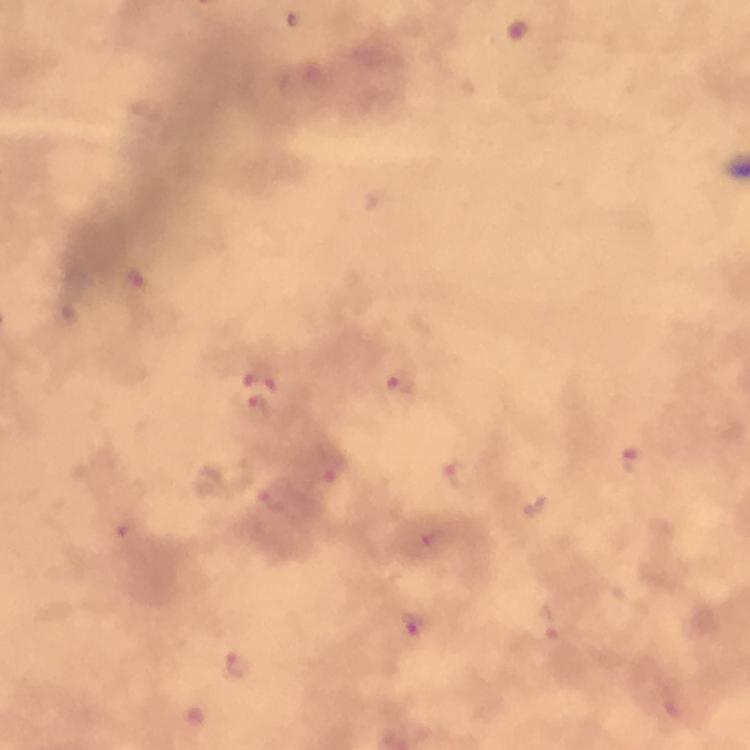
Approximate centers as {x, y} in pixels.
Summary:
  - Malaria parasite locations: {518, 29}, {133, 280}, {260, 377}, {402, 384}, {256, 408}, {630, 460}, {332, 469}, {457, 474}, {274, 502}, {126, 528}, {434, 537}, {415, 623}, {549, 623}, {237, 663}, {671, 710}
  - Image size: 750×750 pixels
  - Preparation: thick smear
  - Context: from a malaria diagnostic workup
  - Stain: Giemsa
  - Cropped from: one field of view
  - Magnification: 100x
  - Immersion oil: used
  - Capture: smartphone camera through the microscope